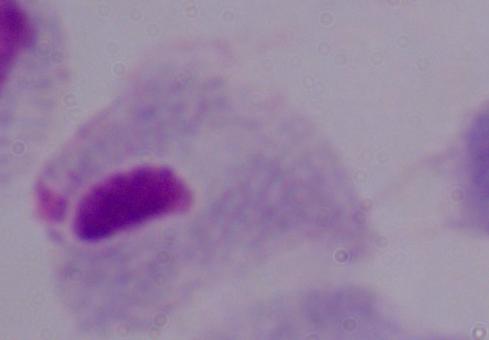
identification = trichomonad
modality = micrograph
magnification = 1000x